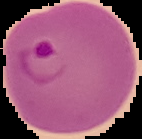

Malaria status: parasitized. Cell region segmented out of the field of view; the surrounding area is masked to black. From a thin blood smear. Image is 142×139 pixels.